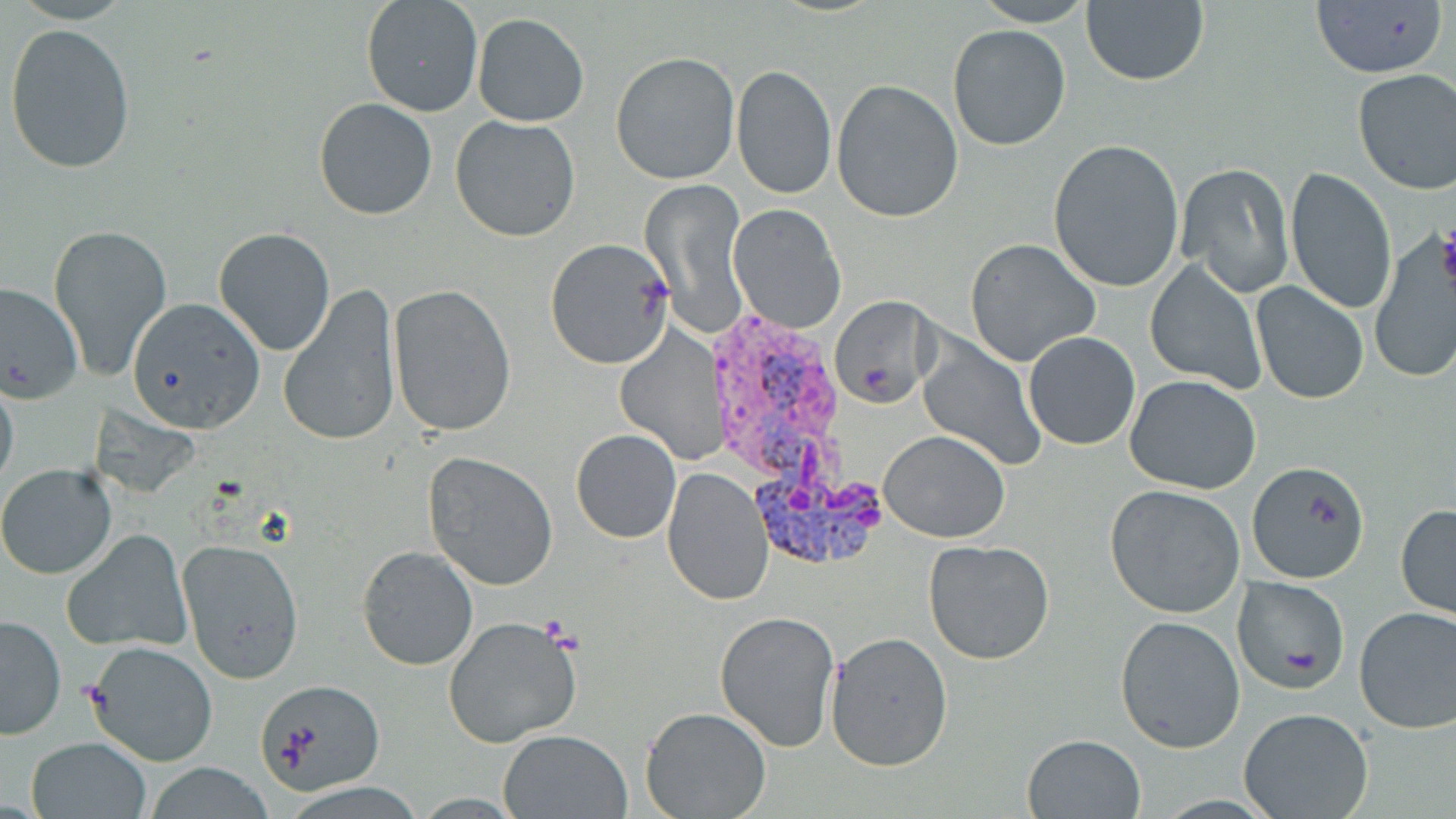
Summary:
  - Coordinate format: approximate bounding boxes as (x1,y1)-(x2,y2) corner pairs in pixels
  - Uninfected red blood cell locations: (361,0)-(483,118), (971,0)-(1096,26), (1308,0)-(1448,80), (1081,1)-(1209,86), (472,12)-(589,127), (4,22)-(137,174), (948,24)-(1069,150), (611,52)-(740,185), (731,64)-(836,200), (1352,69)-(1456,195), (831,79)-(964,223), (314,97)-(437,220), (450,116)-(581,241), (1047,138)-(1185,294), (1175,160)-(1295,297), (1286,167)-(1398,315), (641,177)-(748,340), (729,204)-(846,333), (49,222)-(173,379), (213,227)-(338,356), (965,238)-(1101,365), (545,239)-(676,369), (1367,239)-(1454,384), (1145,259)-(1267,394), (278,281)-(403,447), (1251,281)-(1369,404), (0,282)-(81,405), (387,285)-(517,439), (829,293)-(937,411), (123,297)-(263,434), (1024,331)-(1141,450), (918,335)-(1045,470), (0,372)-(20,493), (1125,374)-(1262,495), (571,429)-(682,544), (879,429)-(1011,542), (424,451)-(558,591), (1248,460)-(1370,583), (0,464)-(117,578), (662,465)-(776,606), (1105,484)-(1246,617), (1395,503)-(1456,621), (63,528)-(193,652), (178,539)-(305,684), (923,539)-(1057,666), (358,546)-(479,670), (1234,576)-(1351,693), (1354,606)-(1456,734), (714,609)-(840,751), (1,614)-(66,739), (442,615)-(583,748), (1115,616)-(1245,752), (827,632)-(953,771), (84,638)-(218,767), (252,677)-(385,797), (641,707)-(770,819), (1238,708)-(1372,819), (498,729)-(632,817), (1023,735)-(1146,818), (26,736)-(152,818), (138,762)-(282,818)
  - Plasmodium vivax-infected red blood cell locations: (730,348)-(893,575)
  - Platelet locations: (1437,225)-(1456,290), (79,679)-(112,712)
  - Slide-level diagnosis: Plasmodium vivax
  - Modality: optical microscopy
  - Magnification: 1000x
  - Preparation: thin blood film
  - Field of view: single
  - Image size: 1456×819 pixels
  - Stain: May-Grünwald-Giemsa